Assess for malaria.
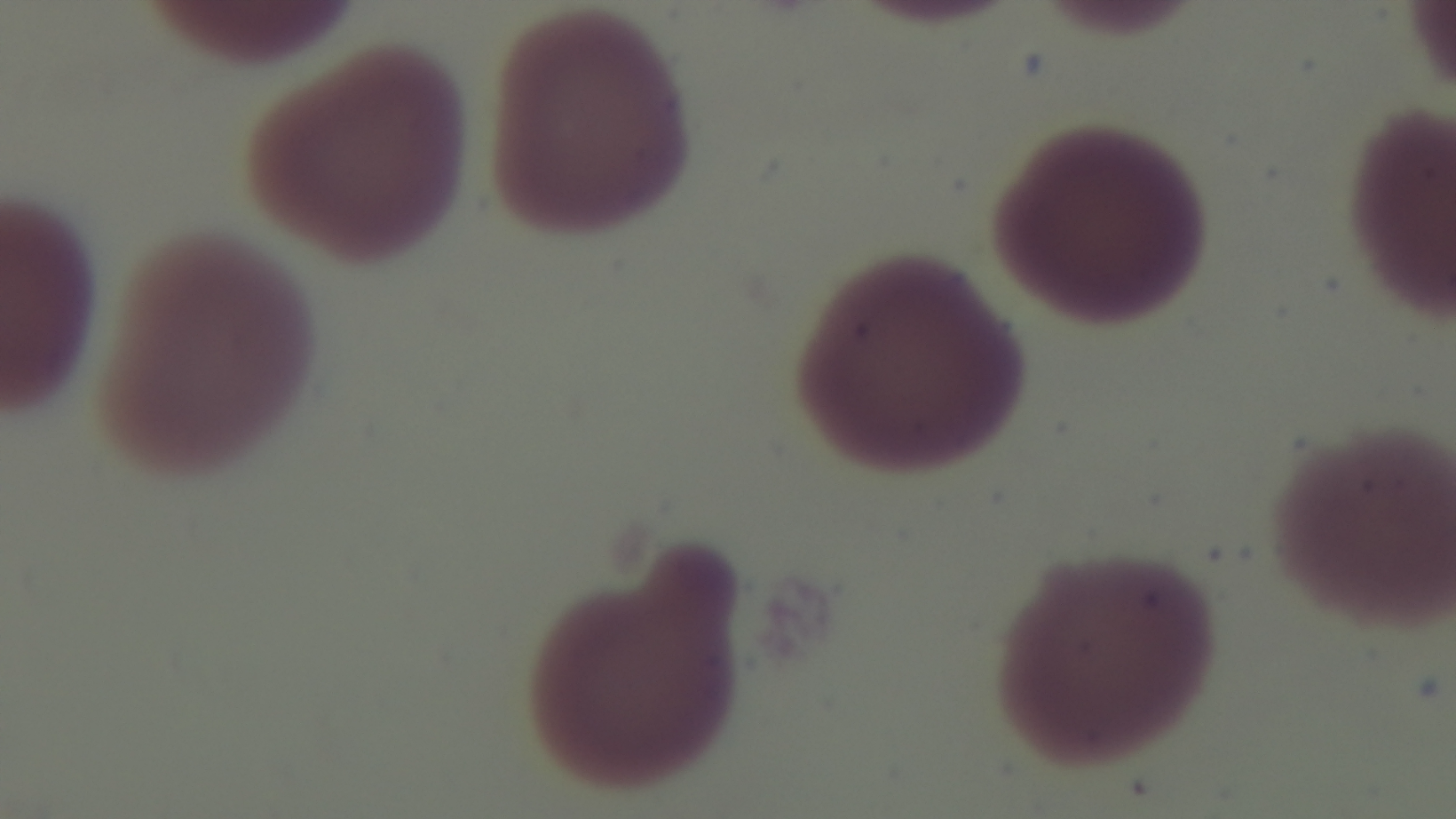
Uninfected.

Summary:
  - Preparation: thin blood film
  - Capture: mounted 4K digital camera
  - Field of view: one from the slide
  - Stain: Giemsa
  - Objective: 100x oil immersion
  - Modality: light microscopy